Mark where platelets are.
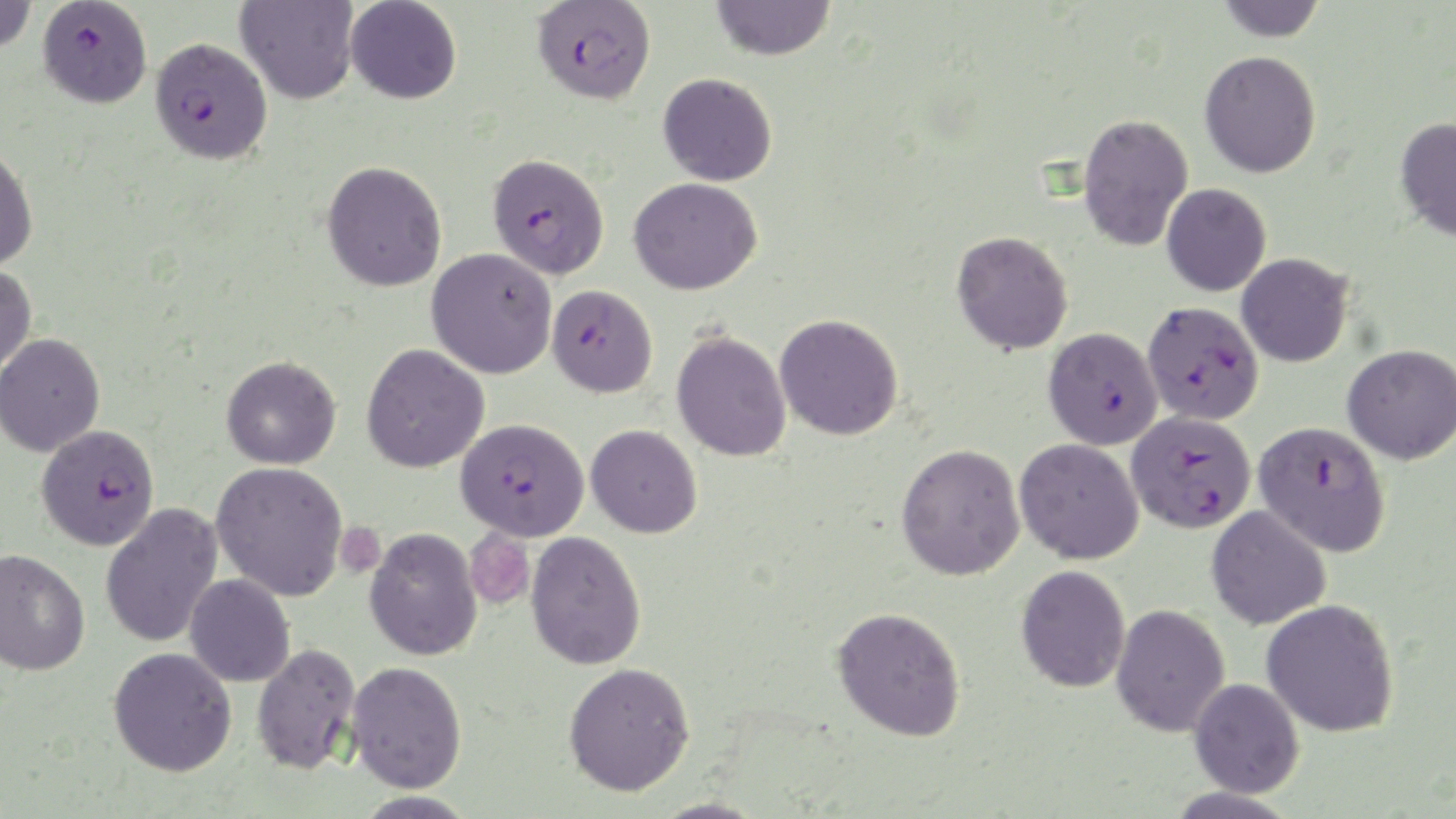

Approximate bounding boxes as [x1, y1, x2, y2] in pixels.
Platelets: [336, 521, 384, 577], [464, 528, 536, 611].

Summary:
  - Uninfected red blood cell locations: [0, 0, 39, 54], [235, 0, 359, 105], [345, 0, 462, 104], [710, 0, 836, 61], [1215, 0, 1328, 42], [1199, 50, 1322, 178], [658, 72, 778, 186], [1077, 113, 1193, 252], [1394, 115, 1456, 242], [0, 144, 39, 272], [321, 160, 448, 292], [629, 176, 763, 295], [1161, 183, 1271, 296], [951, 230, 1074, 355], [427, 248, 557, 379], [1236, 252, 1354, 367], [0, 265, 37, 379], [774, 314, 904, 441], [672, 330, 792, 462], [0, 333, 105, 457], [361, 343, 489, 473], [1342, 343, 1456, 464], [221, 355, 341, 469], [586, 424, 703, 538], [1015, 438, 1144, 564], [896, 443, 1026, 581], [210, 461, 349, 601], [100, 502, 223, 649], [1206, 505, 1331, 630], [365, 528, 481, 661], [526, 531, 646, 670], [0, 548, 90, 676], [1016, 564, 1130, 693], [185, 574, 295, 687], [1262, 599, 1400, 738], [1111, 603, 1230, 737], [831, 605, 966, 740], [251, 641, 361, 774], [108, 646, 237, 776], [346, 660, 467, 792], [563, 661, 696, 796], [1188, 678, 1305, 798]
  - Plasmodium falciparum-infected red blood cell locations: [531, 0, 656, 105], [37, 1, 153, 109], [150, 36, 273, 165], [487, 152, 609, 279], [547, 285, 658, 398], [1142, 300, 1264, 425], [1043, 326, 1163, 450], [1127, 410, 1256, 533], [455, 417, 589, 541], [1254, 421, 1391, 556], [36, 424, 159, 550]
  - Slide-level diagnosis: Plasmodium falciparum
  - Magnification: 1000x
  - Stain: May-Grünwald-Giemsa
  - Preparation: thin blood smear
  - Field of view: one of a larger specimen
  - Modality: optical microscopy
  - Image size: 1456×819 pixels